Give the position of every malaria parasite.
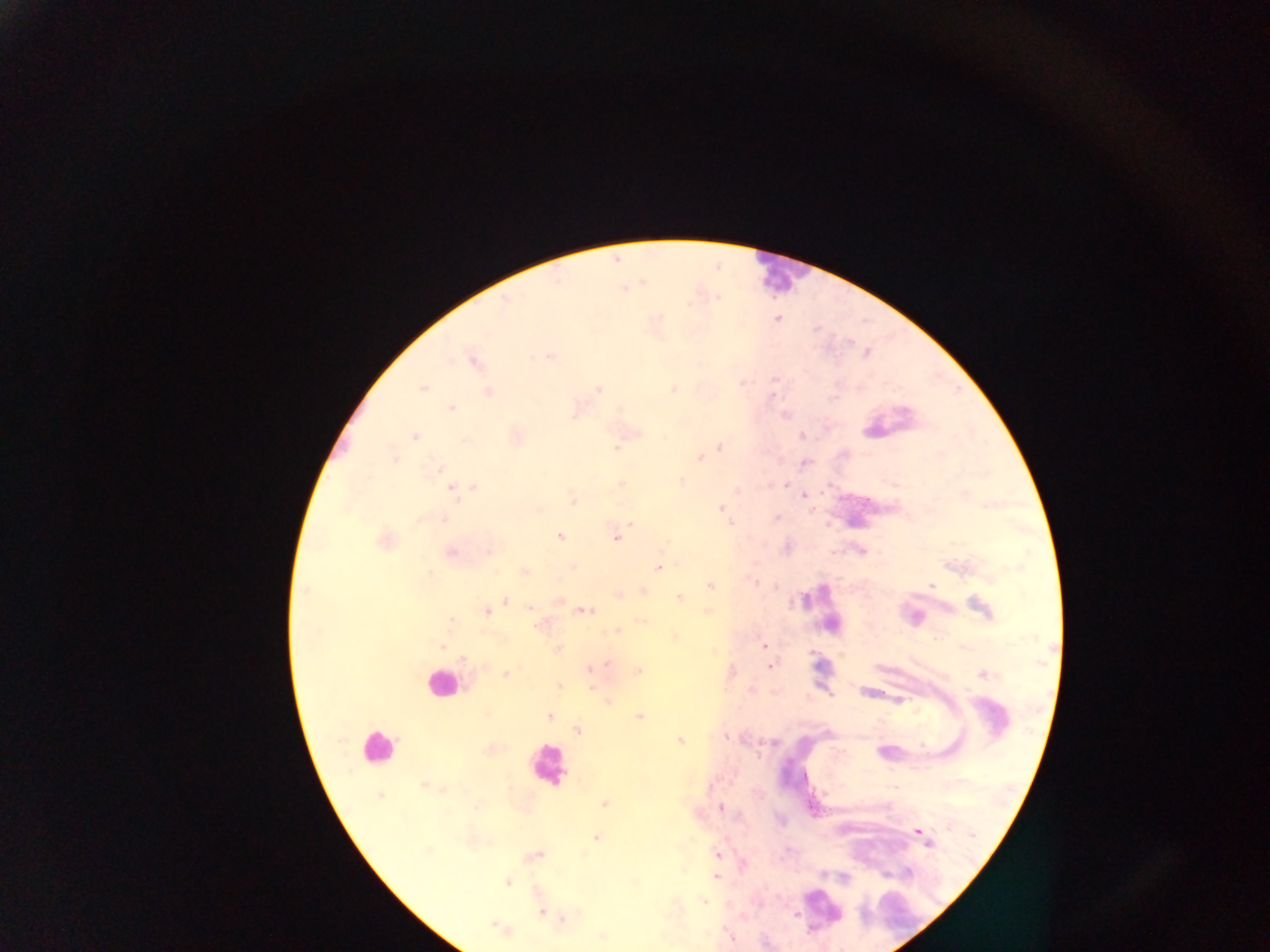
Approximate centers as x y in pixels.
Malaria parasites: 777 318; 550 357; 474 362; 422 388; 674 389; 598 390; 488 393; 773 396; 452 409; 785 415; 802 435; 414 436; 720 447; 617 450; 394 457; 700 457; 806 462; 437 468; 682 481; 622 484; 786 485; 468 487; 473 487; 453 490; 805 494; 573 500; 721 509; 776 518; 630 524; 560 536; 616 537; 658 568; 525 572; 711 585; 932 586; 678 598; 505 600; 530 607; 485 611; 586 611; 709 611; 452 621; 617 631; 764 646; 558 649; 463 659; 607 663; 770 666; 589 669; 638 671; 506 674; 983 674; 558 686; 591 688; 549 716; 639 717; 578 730; 726 736; 680 741; 423 784; 605 803; 720 808; 919 831; 597 838; 927 842; 717 854; 716 876; 508 882; 704 902; 541 912; 796 916; 496 925; 731 938.

field of view = single
capture = mobile-phone photograph through a microscope
country = Ghana
image size = 1270×952 pixels
preparation = thick blood smear
leukocyte locations = approximate centers as x y in pixels: 778 272; 440 683; 376 747; 545 765